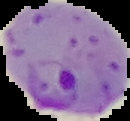
Summary:
  - Result: Plasmodium parasites identified
  - Image type: cell region segmented out of the field of view; surrounding area masked to black
  - Image size: 130×121 pixels
  - Preparation: thin blood film